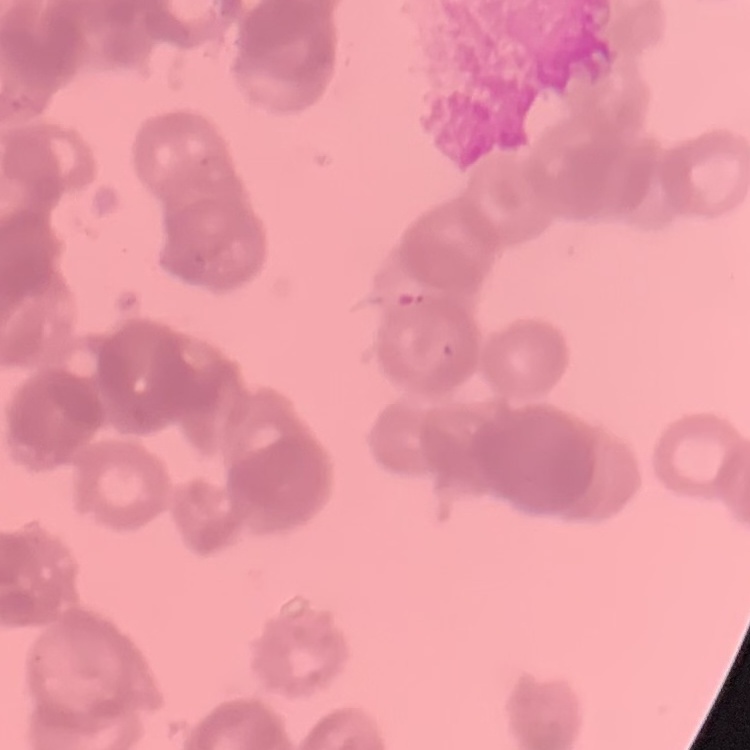

Summary:
  - Red blood cell morphology: rouleaux formation
  - Stain: Field's or Giemsa
  - Preparation: thin blood smear
  - Image type: one tile cut from a larger photomicrograph